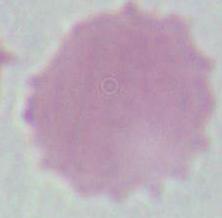
1000x magnification. Photomicrograph. An erythrocyte is seen.